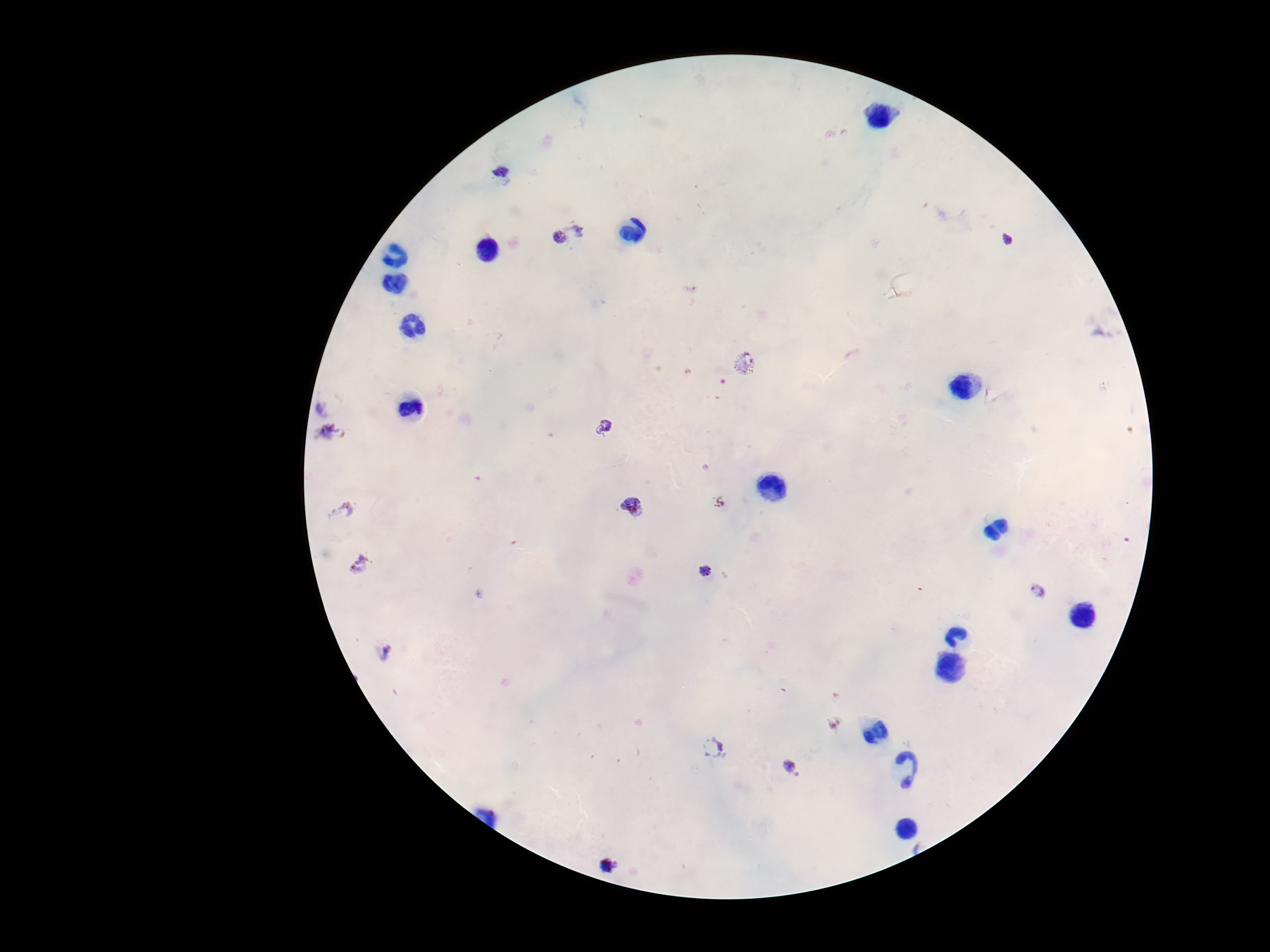

Approximate centers as [x, y] in pixels.
Summary:
  - Plasmodium parasite locations: [502, 175], [580, 225], [557, 239], [1008, 241], [743, 363], [328, 401], [604, 428], [332, 431], [634, 509], [340, 512], [361, 564], [705, 570], [1037, 593], [383, 653], [713, 747], [792, 768], [607, 866]
  - Capture: smartphone camera through the microscope eyepiece
  - Image size: 1270×952 pixels
  - Patient malaria status: positive
  - Field of view: single
  - Magnification: 100x
  - Stain: Giemsa
  - Preparation: thick peripheral-blood smear